Report the malaria status of this cell.
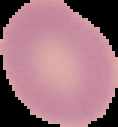

Uninfected.

preparation = thin blood smear
image size = 118×127 pixels
image type = cell region segmented out of the field of view; surrounding area masked to black